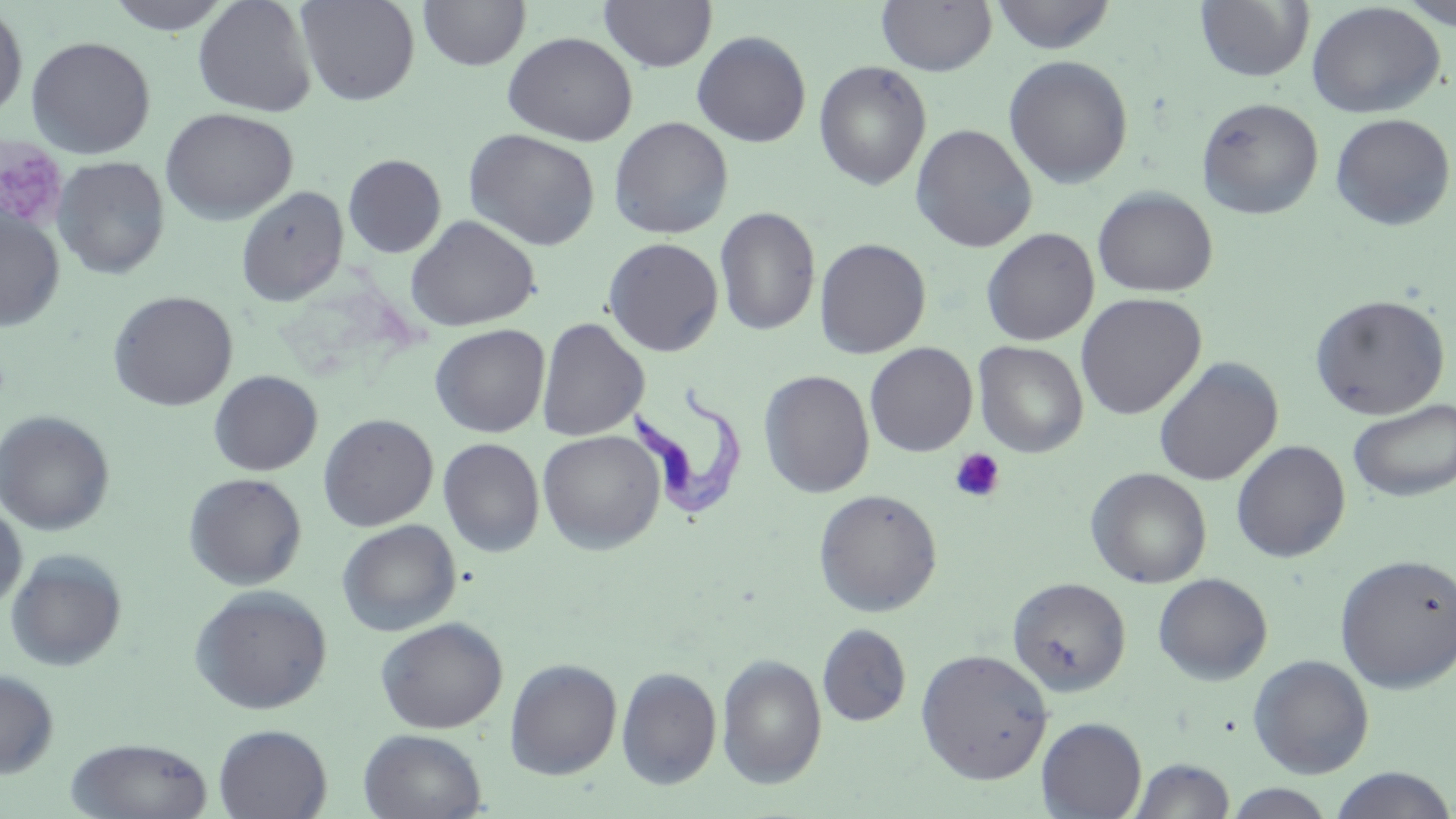
slide_level_diagnosis: Trypanosoma brucei
stain: May-Grünwald-Giemsa
modality: optical microscopy
image_size: 1456×819 pixels
preparation: thin blood film
platelet_locations: 'approximate bounding boxes as (x1,y1)-(x2,y2) corner pairs in pixels: (0,137)-(68,230), (949,448)-(1005,503)'
field_of_view: single
trypanosoma_brucei_locations: 'approximate bounding boxes as (x1,y1)-(x2,y2) corner pairs in pixels: (630,381)-(746,521)'
magnification: 1000x
uninfected_red_blood_cell_locations: 'approximate bounding boxes as (x1,y1)-(x2,y2) corner pairs in pixels: (104,0)-(235,34), (193,0)-(318,117), (296,0)-(420,106), (418,0)-(531,70), (598,0)-(718,73), (990,0)-(1118,54), (876,1)-(997,75), (1194,1)-(1314,83), (1307,2)-(1445,118), (0,3)-(28,120), (1396,4)-(1456,33), (691,30)-(812,147), (502,31)-(637,145), (25,35)-(156,159), (1003,55)-(1134,189), (814,61)-(932,190), (1196,97)-(1324,220), (161,107)-(298,224), (1330,113)-(1455,231), (608,116)-(733,239), (911,124)-(1037,253), (463,128)-(601,251), (342,154)-(446,258), (52,156)-(170,280), (236,186)-(348,307), (1093,187)-(1218,297), (715,206)-(821,337), (0,212)-(65,331), (405,215)-(540,332), (981,228)-(1099,346), (602,237)-(724,357), (814,237)-(932,359), (108,290)-(238,412), (1075,293)-(1206,420), (1310,294)-(1450,419), (537,317)-(649,441), (429,323)-(550,438), (974,341)-(1089,457), (865,342)-(978,457), (1153,357)-(1283,487), (758,369)-(875,498), (209,371)-(322,476), (1347,398)-(1456,502), (0,410)-(115,535), (318,413)-(438,531), (537,429)-(666,554), (437,437)-(545,557), (1231,440)-(1350,562), (1085,467)-(1212,588), (184,473)-(307,590), (813,488)-(942,617), (0,502)-(27,612), (337,519)-(461,635), (5,549)-(128,672), (1335,553)-(1456,693), (1153,572)-(1273,685), (1008,576)-(1131,696), (189,584)-(333,715), (375,617)-(508,733), (816,623)-(912,727), (915,648)-(1053,784), (716,653)-(827,788), (1248,654)-(1374,779), (504,658)-(622,779), (617,666)-(721,790), (0,669)-(59,778), (1036,717)-(1147,819), (213,724)-(332,818), (359,728)-(487,819), (66,737)-(214,819), (1129,757)-(1236,819), (1328,766)-(1456,819), (1220,783)-(1338,818)'